Comment on the morphology of the erythrocytes.
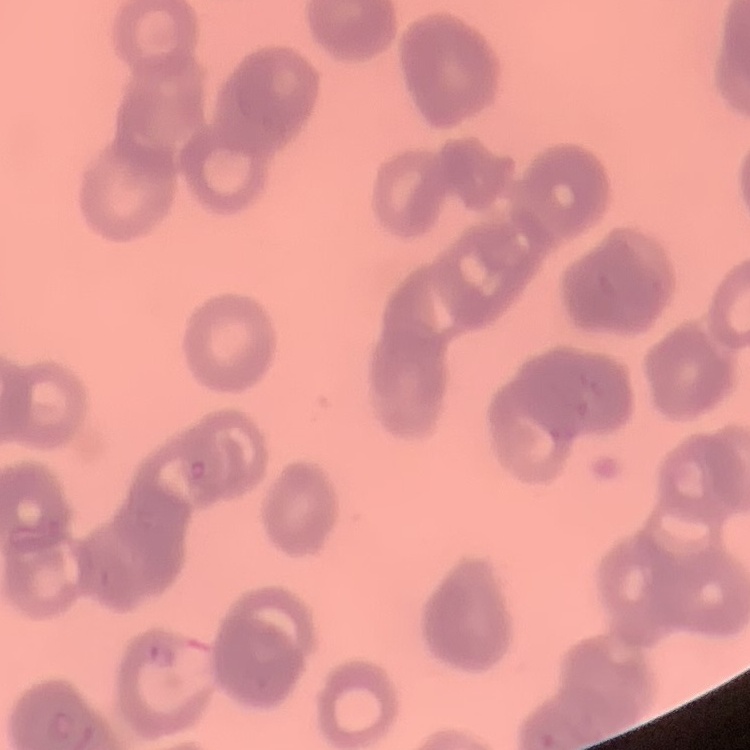

Rouleaux formation.

preparation = thin blood smear
image type = square crop of a larger photomicrograph
stain = Field's or Giemsa